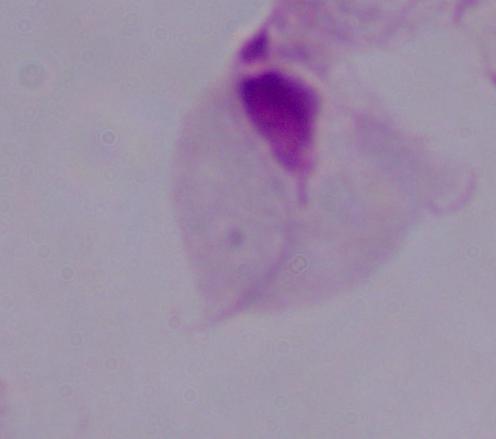
Summary:
  - Magnification: 1000x
  - Identification: trichomonad
  - Modality: micrograph